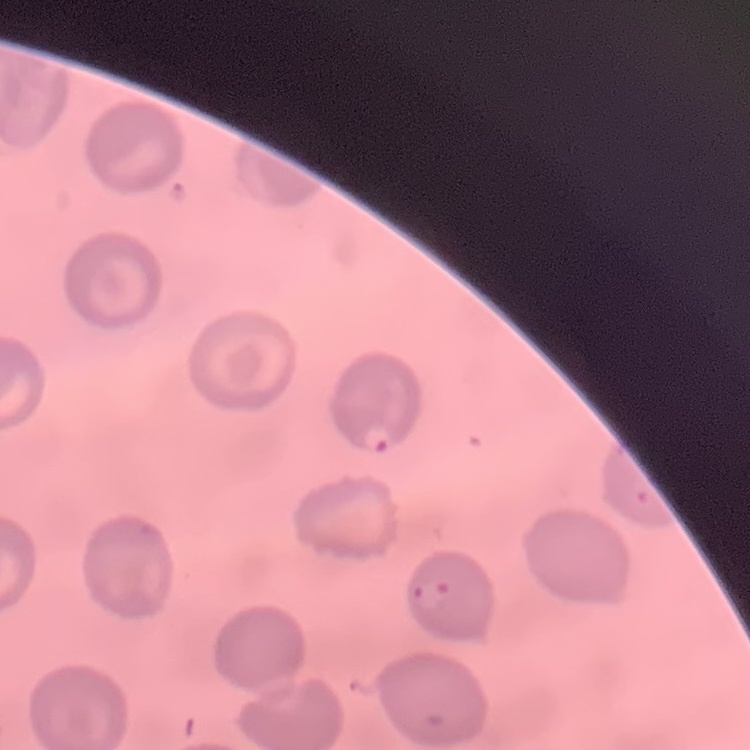
red_blood_cell_morphology: no rouleaux formation
stain: Field's or Giemsa
image_type: one tile cut from a larger photomicrograph
preparation: thin blood film